Assess this cell for malaria.
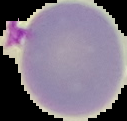
It is uninfected.

Summary:
  - Preparation: thin blood smear
  - Image size: 127×121 pixels
  - Image type: segmented cell region with the area outside set to black